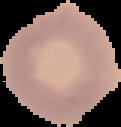

image type = segmented cell region with the area outside set to black
result = no Plasmodium parasites seen
image size = 121×127 pixels
preparation = thin blood smear